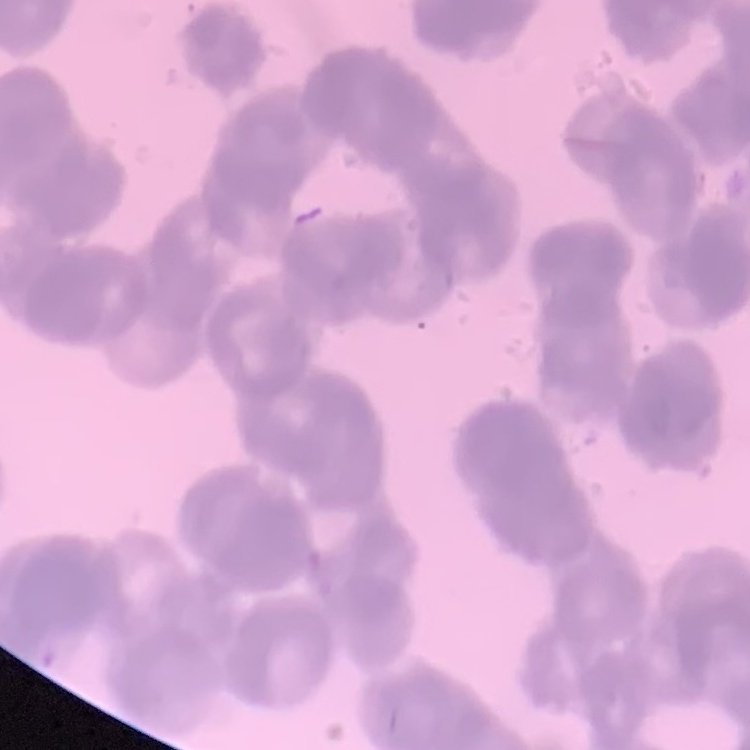

Summary:
  - Erythrocyte morphology: rouleaux formation
  - Stain: Field's or Giemsa
  - Image type: one tile cut from a larger photomicrograph
  - Preparation: thin blood smear